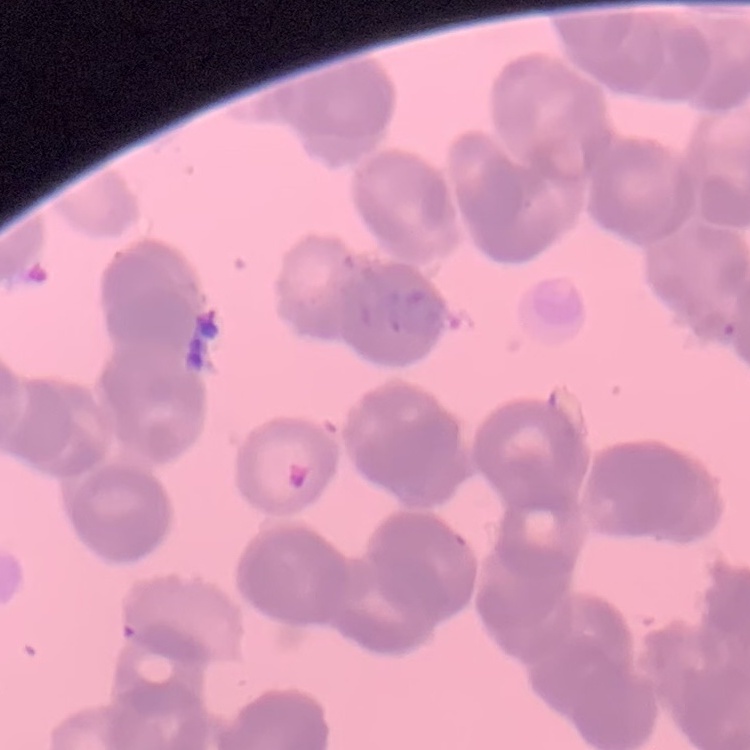
Summary:
  - Red blood cell morphology: rouleaux formation
  - Stain: Field's or Giemsa
  - Preparation: thin blood smear
  - Image type: one tile cut from a larger photomicrograph